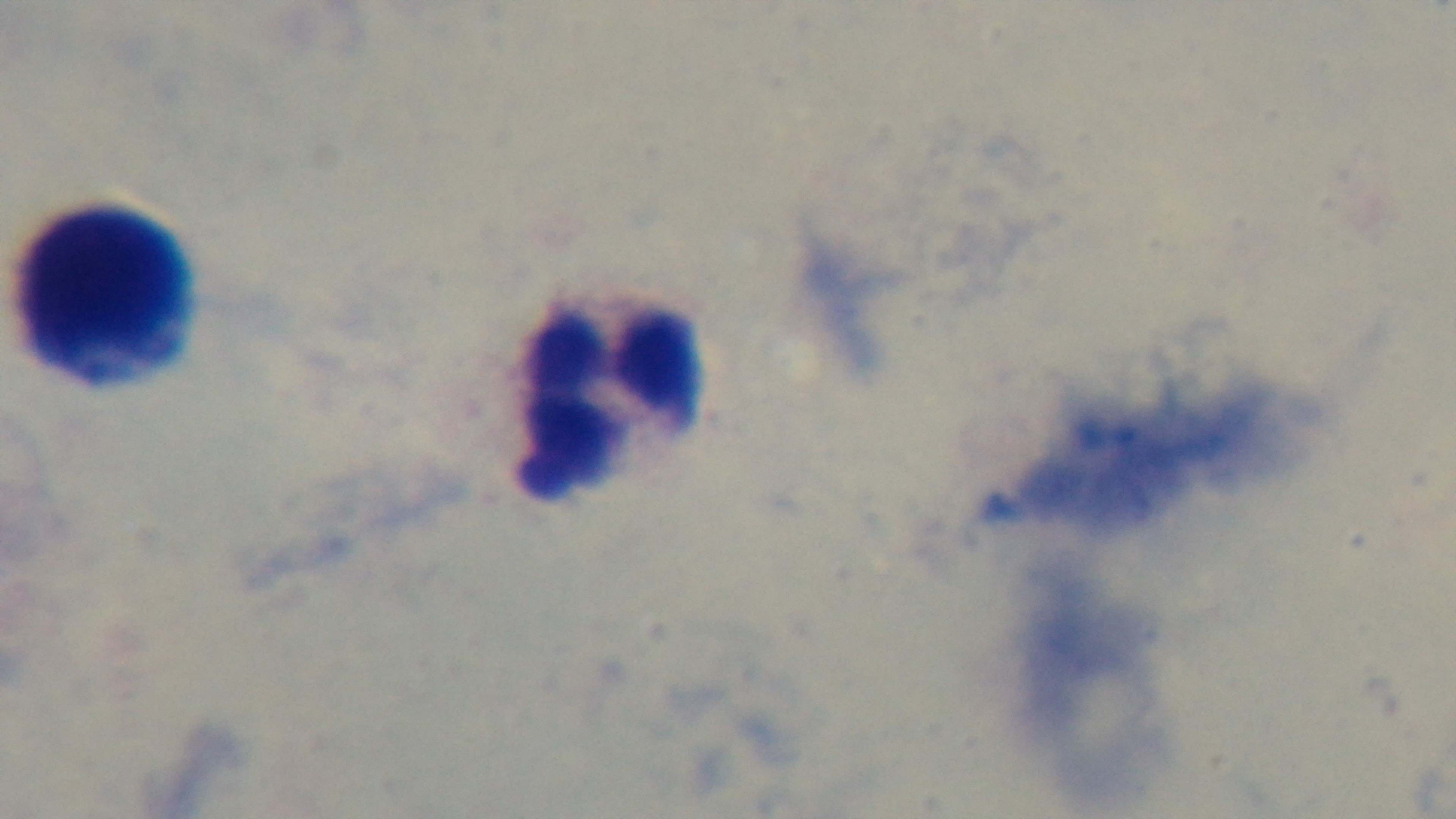
{
  "field_of_view": "single",
  "preparation": "thick",
  "modality": "light microscopy",
  "stain": "Giemsa",
  "objective": "100x oil immersion",
  "malaria_status": "negative",
  "capture": "mounted 4K digital camera"
}